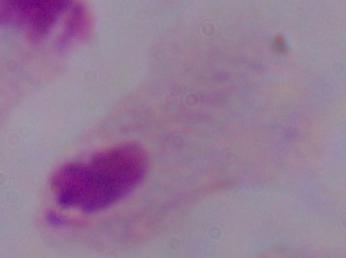
identification = trichomonad
modality = micrograph
magnification = 1000x